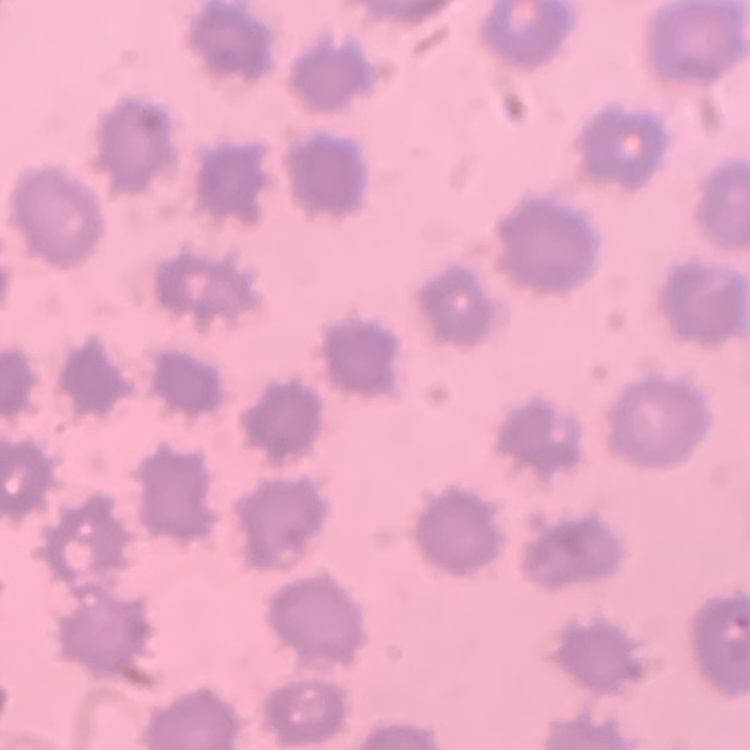

Summary:
  - Erythrocyte morphology: no rouleaux formation
  - Stain: Field's or Giemsa
  - Image type: one tile cut from a larger photomicrograph
  - Preparation: thin blood film